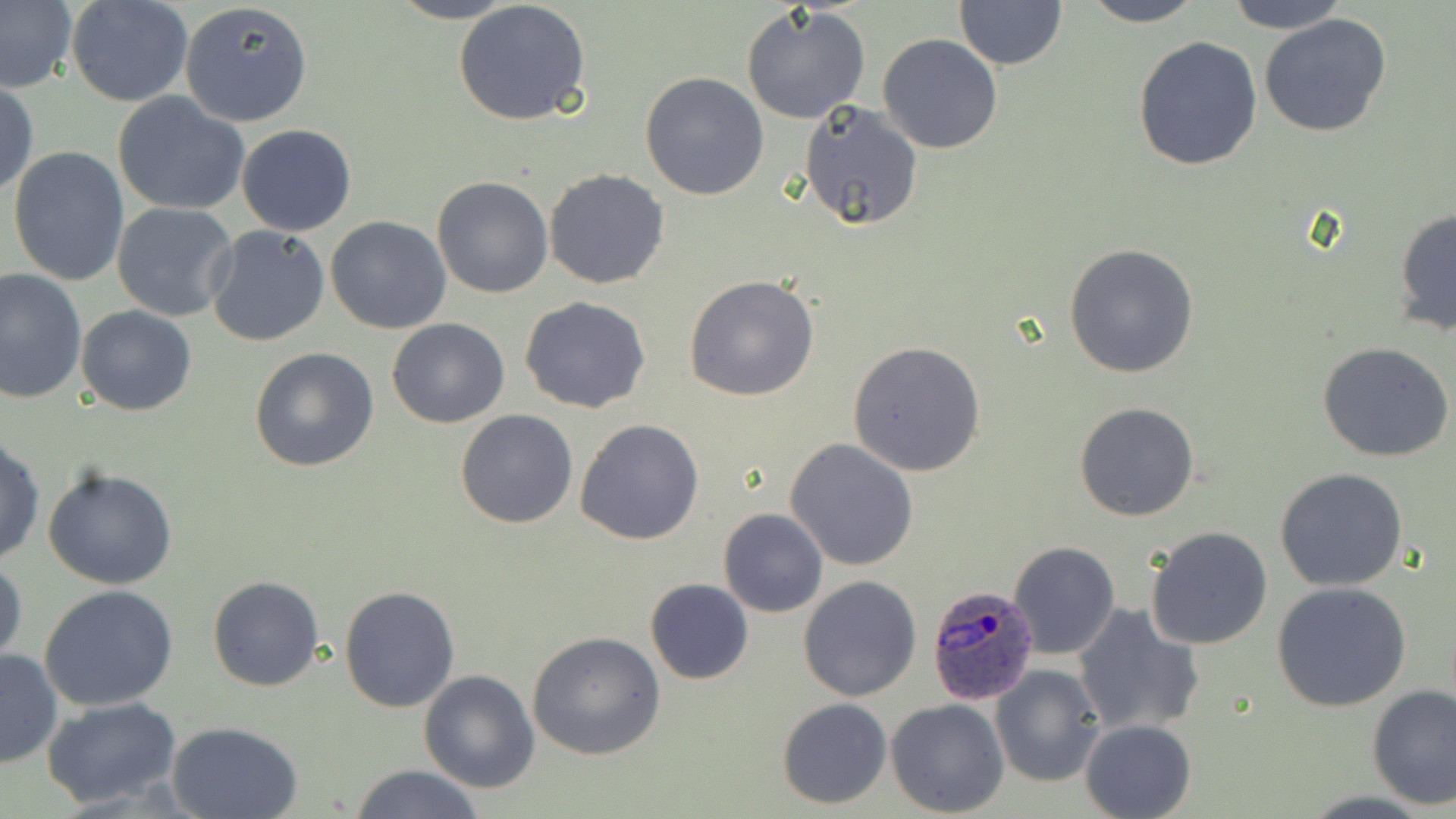
Approximate bounding boxes as [x1, y1, x2, y2] in pixels. Uninfected red blood cell locations: [0, 0, 79, 95], [65, 0, 194, 106], [386, 0, 521, 24], [1076, 0, 1207, 27], [1221, 0, 1350, 34], [453, 1, 592, 125], [178, 2, 312, 128], [954, 2, 1068, 69], [740, 6, 872, 127], [1259, 13, 1392, 137], [877, 35, 1003, 154], [1132, 35, 1264, 173], [641, 72, 769, 200], [1, 80, 38, 201], [111, 91, 251, 217], [799, 100, 924, 231], [236, 124, 358, 236], [6, 145, 130, 289], [543, 168, 670, 290], [431, 175, 555, 298], [111, 201, 238, 321], [1393, 208, 1455, 336], [326, 217, 452, 334], [204, 225, 331, 348], [1065, 242, 1200, 378], [0, 267, 86, 403], [683, 275, 819, 402], [519, 295, 651, 414], [78, 306, 197, 415], [385, 318, 510, 428], [847, 340, 988, 476], [1317, 342, 1456, 463], [248, 346, 379, 472], [1074, 401, 1200, 521], [456, 410, 578, 528], [575, 418, 705, 545], [0, 435, 44, 568], [786, 438, 918, 571], [43, 468, 178, 590], [1274, 468, 1409, 592], [718, 508, 828, 617], [1145, 526, 1275, 649], [1009, 541, 1120, 659], [0, 554, 26, 671], [207, 575, 326, 692], [798, 576, 923, 702], [645, 579, 754, 685], [1272, 582, 1411, 713], [39, 584, 179, 711], [338, 585, 459, 713], [1072, 605, 1204, 737], [526, 631, 666, 760], [0, 649, 62, 769], [989, 664, 1104, 787], [419, 670, 540, 793], [1367, 684, 1455, 808], [41, 696, 183, 810], [777, 698, 891, 808], [886, 698, 1009, 817], [1079, 719, 1198, 819], [168, 721, 304, 819], [349, 764, 486, 819]. Plasmodium ovale-infected red blood cell locations: [927, 582, 1040, 705]. Slide-level diagnosis: Plasmodium ovale. Optical microscopy. 1000x magnification. Thin blood smear. Image is 1456×819 pixels. May-Grünwald-Giemsa stain. One field of a larger specimen.